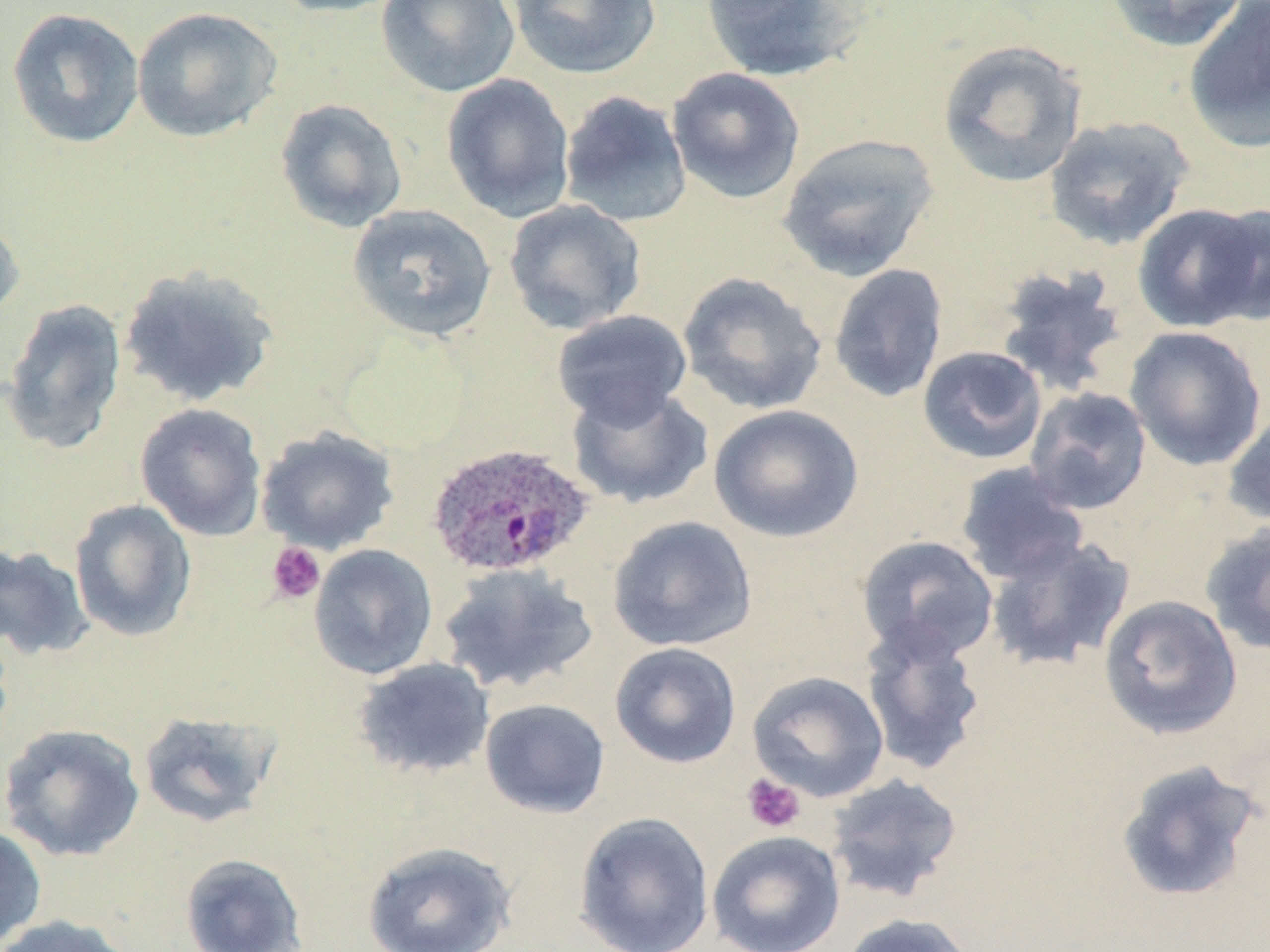

Plasmodium ovale-infected red blood cell locations = approximate bounding boxes as (x1, y1, x2, y2) in pixels: (425, 442, 594, 580)
slide-level diagnosis = Plasmodium ovale
field of view = single
preparation = thin blood film
stain = May-Grünwald-Giemsa
uninfected red blood cell locations = approximate bounding boxes as (x1, y1, x2, y2) in pixels: (265, 0, 408, 18), (376, 0, 520, 98), (508, 0, 661, 79), (699, 0, 868, 83), (1105, 0, 1249, 52), (1184, 1, 1270, 152), (131, 6, 282, 144), (6, 7, 145, 149), (936, 39, 1088, 188), (667, 67, 805, 204), (441, 73, 576, 223), (559, 90, 692, 228), (274, 98, 408, 233), (1043, 115, 1195, 251), (777, 133, 940, 282), (503, 199, 646, 334), (1202, 202, 1269, 326), (1133, 203, 1265, 332), (347, 204, 497, 343), (0, 211, 25, 325), (828, 263, 949, 404), (993, 264, 1131, 399), (117, 265, 280, 408), (677, 271, 827, 415), (1, 299, 129, 454), (551, 309, 693, 429), (1124, 325, 1267, 471), (918, 345, 1048, 465), (567, 384, 714, 509), (1024, 386, 1153, 515), (135, 402, 268, 541), (709, 404, 864, 542), (1223, 404, 1270, 528), (255, 426, 399, 554), (954, 462, 1090, 586), (69, 499, 197, 642), (607, 515, 757, 652), (1200, 521, 1270, 657), (985, 534, 1136, 672), (857, 535, 999, 663), (0, 543, 95, 662), (308, 544, 438, 680), (438, 563, 599, 695), (1098, 594, 1243, 740), (859, 620, 988, 777), (0, 626, 15, 759), (609, 642, 741, 769), (352, 657, 495, 779), (746, 670, 890, 802), (479, 697, 611, 819), (137, 709, 281, 828), (0, 723, 146, 862), (1114, 758, 1264, 904), (826, 773, 964, 902), (573, 811, 715, 951), (0, 823, 47, 950), (706, 831, 846, 952), (361, 840, 517, 951), (179, 853, 308, 952), (838, 912, 978, 952), (0, 915, 135, 952)
image size = 1270×952 pixels
platelet locations = approximate bounding boxes as (x1, y1, x2, y2) in pixels: (266, 541, 326, 604), (742, 774, 805, 833)
modality = optical microscopy
magnification = 1000x